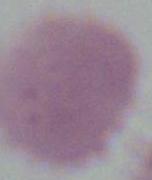 An erythrocyte is seen. Micrograph. 1000x magnification.